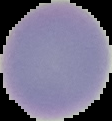 Result: no Plasmodium parasites detected. Cell region segmented out of the field of view; the surrounding area is masked to black. Image is 112×121 pixels. From a thin blood film.